Locate every Plasmodium vivax-infected red blood cell.
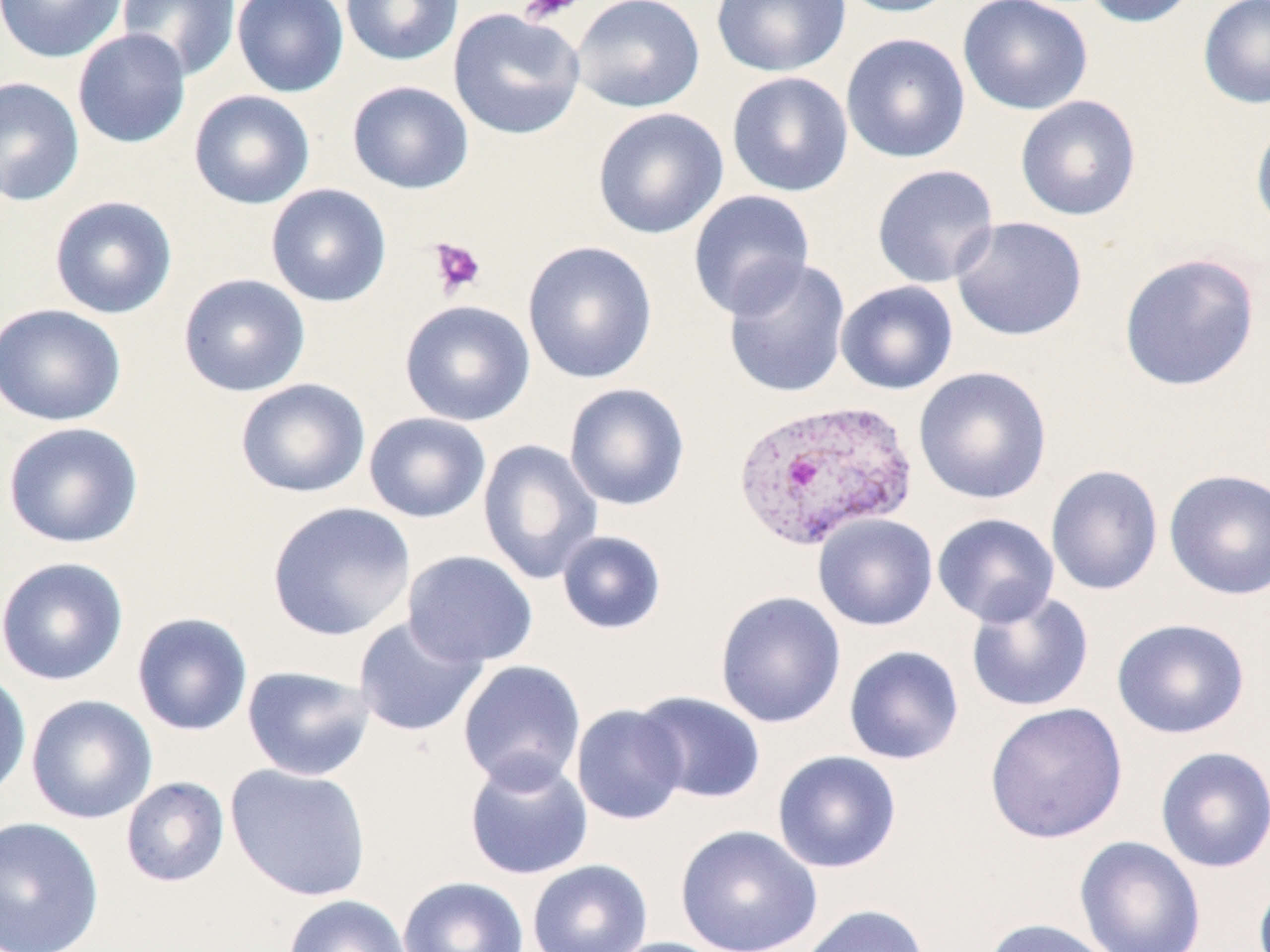

Approximate bounding boxes as (x1,y1)-(x2,y2) corner pairs in pixels.
Plasmodium vivax-infected red blood cells: (731,399)-(917,553).

Summary:
  - Platelet locations: (517,0)-(585,25), (426,238)-(487,298)
  - Uninfected red blood cell locations: (0,0)-(128,63), (117,0)-(241,81), (231,0)-(349,97), (340,0)-(464,66), (571,0)-(705,112), (711,0)-(852,77), (834,0)-(964,18), (957,0)-(1093,116), (1080,0)-(1200,28), (1198,0)-(1270,109), (448,8)-(585,140), (71,29)-(191,149), (840,32)-(971,164), (727,72)-(854,197), (0,76)-(85,207), (347,80)-(474,194), (189,89)-(315,209), (1015,95)-(1142,221), (592,107)-(729,240), (1250,117)-(1270,237), (871,164)-(1000,288), (266,183)-(392,308), (687,190)-(816,320), (49,195)-(177,319), (950,216)-(1088,342), (522,240)-(658,385), (1118,252)-(1260,392), (722,258)-(852,400), (178,273)-(311,397), (836,280)-(958,395), (399,299)-(536,426), (0,302)-(126,426), (913,366)-(1052,505), (234,377)-(371,498), (563,382)-(690,511), (363,411)-(491,523), (2,421)-(144,549), (477,438)-(603,585), (1045,464)-(1164,596), (1163,468)-(1270,601), (266,501)-(416,641), (932,512)-(1060,627), (813,513)-(938,631), (556,530)-(667,635), (402,549)-(539,668), (0,555)-(129,686), (965,589)-(1095,713), (714,590)-(847,729), (131,612)-(253,737), (352,615)-(487,737), (1111,618)-(1250,739), (843,644)-(964,766), (457,659)-(587,791), (241,665)-(375,782), (0,668)-(32,802), (633,690)-(767,804), (25,694)-(158,824), (984,702)-(1128,844), (570,703)-(689,825), (1155,746)-(1270,873), (771,750)-(902,874), (463,755)-(594,881), (225,763)-(372,901), (120,776)-(230,887), (0,815)-(104,952), (674,824)-(823,952), (1074,835)-(1206,952), (527,859)-(652,952), (397,876)-(530,952), (282,894)-(412,952), (797,903)-(930,952), (980,918)-(1118,952), (601,936)-(730,952)
  - Slide-level diagnosis: Plasmodium vivax
  - Magnification: 1000x
  - Stain: May-Grünwald-Giemsa
  - Modality: optical microscopy
  - Preparation: thin blood smear
  - Image size: 1270×952 pixels
  - Field of view: one of a larger specimen